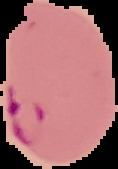

Malaria status: parasitized. Cell region segmented out of the field of view; the surrounding area is masked to black. From a thin blood film. Image is 118×169 pixels.